Find the red blood cells that are infected with P. falciparum, and any of indeterminate infection status.
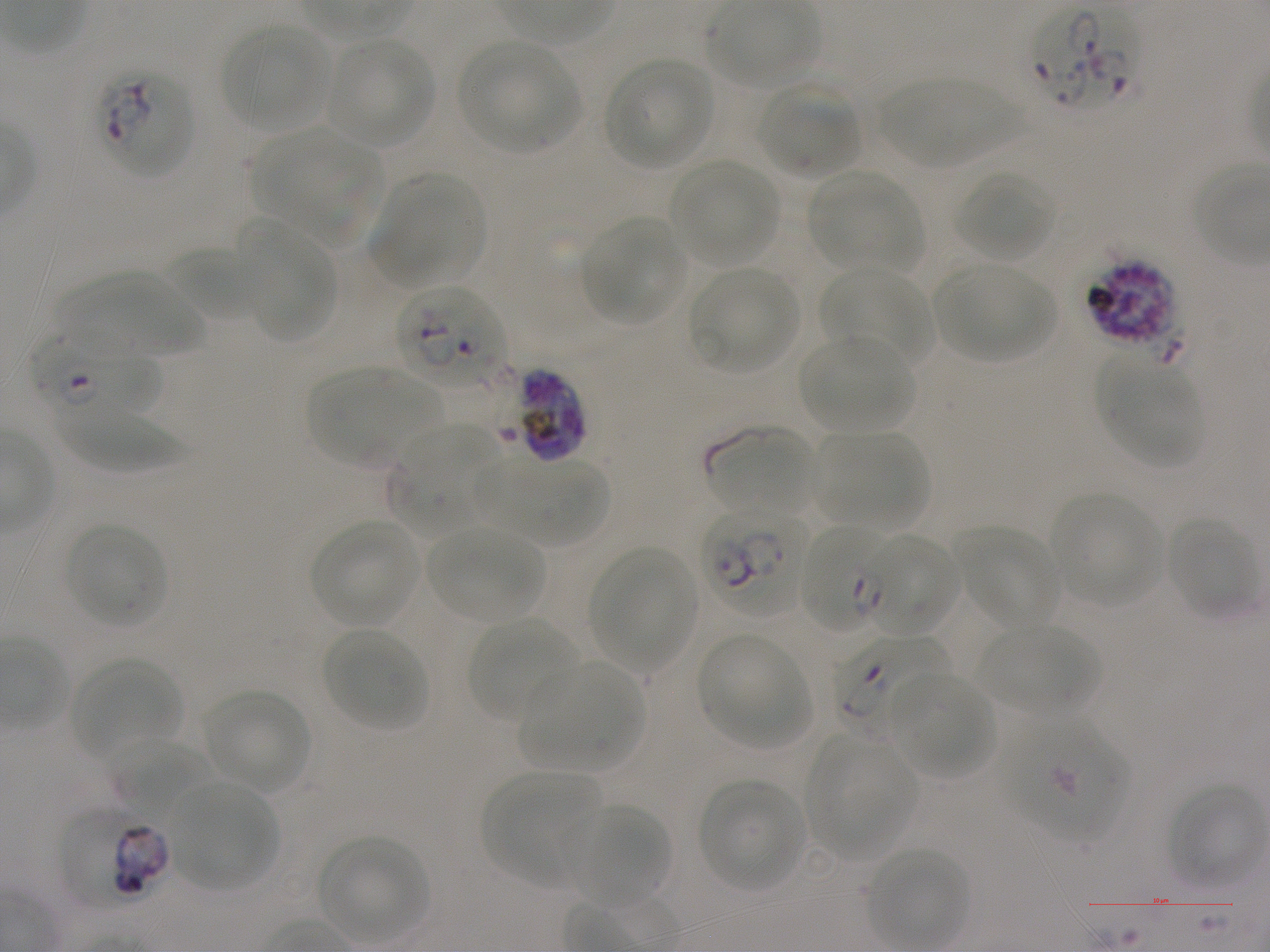
Approximate bounding boxes as {x1, y1, x2, y2} in pixels. Not every red blood cell is marked. A life-cycle stage — or a range of stages, where the recorded stages span more than one — follows each staged infected red blood cell.
Infected red blood cells: {1029, 3, 1142, 109}; {96, 70, 193, 178}; {1084, 259, 1177, 347} late schizont; {394, 284, 506, 388}; {26, 336, 166, 421} ring; {507, 368, 587, 463} schizont; {699, 506, 807, 618}; {798, 525, 892, 634} ring; {831, 633, 950, 737} ring.
Red blood cells of indeterminate infection status: {858, 532, 961, 638}, {1004, 720, 1128, 840}, {60, 810, 145, 908}, {108, 822, 171, 897}.

Summary:
  - Locations of uninfected red blood cells: {221, 24, 332, 131}, {325, 37, 435, 147}, {459, 42, 580, 152}, {605, 58, 715, 170}, {881, 76, 1019, 168}, {755, 86, 860, 178}, {253, 129, 383, 248}, {670, 159, 779, 266}, {955, 169, 1055, 262}, {808, 170, 919, 272}, {371, 173, 485, 287}, {583, 217, 685, 325}, {237, 220, 336, 343}, {166, 245, 266, 320}, {932, 264, 1055, 362}, {688, 267, 801, 373}, {821, 267, 933, 369}, {58, 272, 203, 358}, {798, 335, 917, 432}, {1102, 359, 1203, 466}, {307, 367, 436, 466}, {60, 403, 181, 472}, {707, 426, 817, 519}, {388, 427, 500, 534}, {817, 431, 925, 529}, {487, 457, 608, 544}, {1050, 491, 1164, 605}, {1166, 518, 1258, 619}, {310, 519, 422, 625}, {64, 523, 167, 627}, {427, 527, 544, 621}, {958, 528, 1060, 630}, {588, 546, 695, 670}, {467, 618, 580, 723}, {980, 623, 1096, 714}, {321, 627, 431, 733}, {697, 634, 810, 747}, {69, 657, 183, 760}, {520, 662, 644, 771}, {887, 671, 996, 778}, {201, 688, 313, 793}, {806, 736, 916, 860}, {108, 738, 213, 823}, {482, 773, 598, 888}, {698, 778, 807, 892}, {168, 780, 278, 890}, {1168, 784, 1264, 889}, {564, 804, 671, 909}, {317, 835, 428, 942}, {867, 848, 968, 949}
  - Life-cycle stages observed: ring, schizont
  - Image size: 1270×952 pixels
  - Stain: Giemsa
  - Field of view: one from this slide
  - Donor blood group: A+
  - Culture: static in-vitro P. falciparum strain NF54
  - Preparation: thin blood film
  - Objective: 100x, oil immersion, numerical aperture 1.25